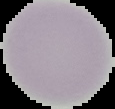
result = negative for Plasmodium parasites
image type = segmented cell region with the area outside set to black
preparation = thin blood film
image size = 115×109 pixels